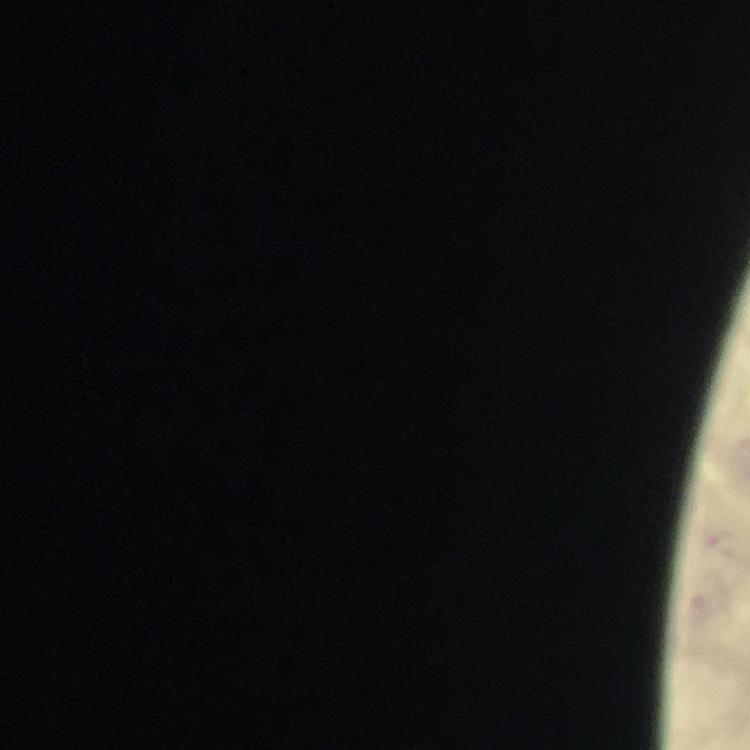

preparation = thick blood smear
context = from a diagnostic examination for malaria
immersion oil = applied
stain = Giemsa
cropped from = one field of view
magnification = 100x
Plasmodium parasite locations = approximate object centers, in pixels from the top-left corner: (x=722, y=542)
image size = 750×750 pixels
capture = smartphone photograph through a microscope